Give the position of every malaria parasite.
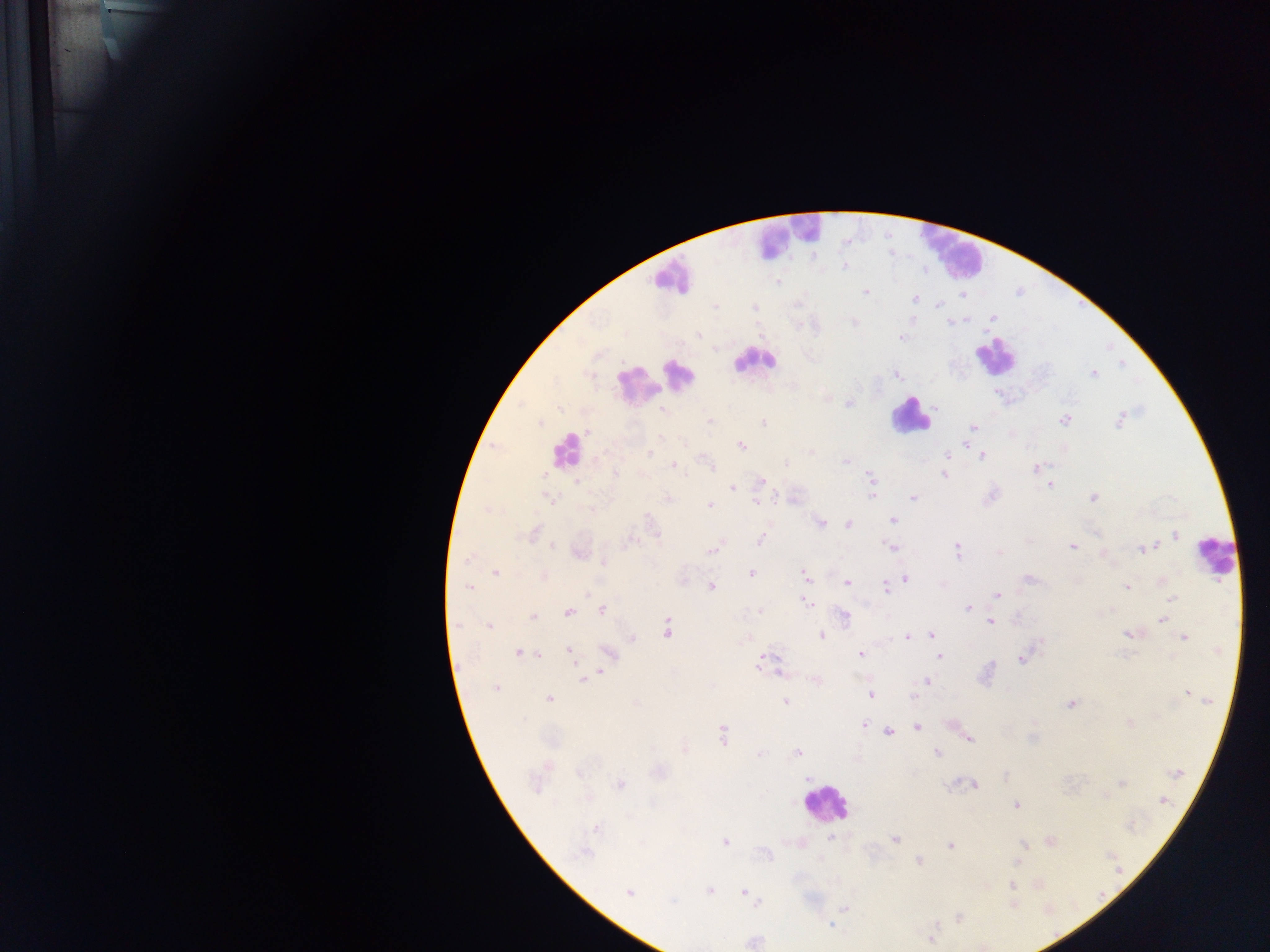
Approximate centers as {x, y} in pixels.
Malaria parasites: {844, 267}, {779, 282}, {865, 292}, {963, 296}, {915, 299}, {939, 305}, {715, 307}, {993, 317}, {965, 319}, {853, 321}, {949, 322}, {699, 335}, {902, 337}, {715, 349}, {1094, 374}, {896, 375}, {828, 399}, {849, 403}, {935, 407}, {559, 409}, {664, 411}, {1120, 419}, {1064, 420}, {710, 421}, {541, 423}, {763, 423}, {973, 428}, {587, 432}, {660, 437}, {684, 444}, {966, 444}, {741, 446}, {810, 452}, {650, 454}, {947, 455}, {982, 456}, {845, 461}, {786, 463}, {673, 465}, {709, 465}, {1036, 469}, {616, 473}, {543, 474}, {944, 475}, {871, 478}, {761, 481}, {577, 482}, {1050, 485}, {732, 488}, {872, 495}, {777, 497}, {913, 497}, {1093, 497}, {549, 499}, {669, 499}, {756, 502}, {709, 505}, {590, 509}, {486, 510}, {648, 518}, {894, 520}, {820, 523}, {847, 525}, {534, 533}, {1175, 534}, {760, 539}, {1029, 541}, {629, 542}, {553, 546}, {890, 546}, {1072, 546}, {1146, 548}, {713, 549}, {957, 551}, {998, 553}, {579, 554}, {469, 557}, {604, 562}, {495, 573}, {751, 573}, {805, 575}, {544, 576}, {905, 579}, {1027, 579}, {683, 581}, {1164, 581}, {847, 583}, {712, 587}, {885, 587}, {1127, 587}, {469, 588}, {587, 593}, {997, 595}, {1172, 598}, {807, 603}, {968, 608}, {1112, 610}, {602, 611}, {760, 611}, {569, 612}, {844, 616}, {533, 618}, {1162, 619}, {990, 622}, {457, 625}, {489, 626}, {667, 630}, {932, 635}, {1130, 635}, {821, 636}, {907, 637}, {1185, 638}, {632, 639}, {569, 650}, {518, 652}, {608, 653}, {538, 654}, {861, 654}, {940, 656}, {1021, 659}, {758, 663}, {600, 672}, {583, 679}, {816, 681}, {926, 681}, {496, 688}, {1189, 694}, {871, 696}, {914, 696}, {549, 699}, {1204, 700}, {785, 701}, {1070, 703}, {1130, 722}, {864, 725}, {917, 727}, {889, 732}, {722, 735}, {969, 739}, {685, 750}, {760, 753}, {798, 753}, {937, 753}, {579, 772}, {660, 772}, {1176, 772}, {808, 778}, {1122, 783}, {536, 784}, {620, 784}, {972, 784}, {1162, 800}, {1017, 805}, {596, 829}, {830, 838}, {894, 839}, {1051, 841}, {725, 842}, {1024, 844}, {951, 845}, {762, 853}, {583, 854}, {918, 861}, {1017, 862}, {1012, 885}, {709, 890}, {744, 892}, {629, 893}, {757, 902}, {1013, 904}, {844, 908}, {958, 917}, {831, 925}, {933, 938}, {753, 941}.

Summary:
  - Leukocyte locations: {786, 237}, {950, 250}, {670, 277}, {994, 355}, {753, 360}, {680, 373}, {654, 378}, {636, 386}, {910, 416}, {566, 450}, {1216, 555}, {826, 804}
  - Country: Ghana
  - Image size: 1270×952 pixels
  - Field of view: single
  - Capture: mobile-phone photograph through a microscope
  - Preparation: thick blood film